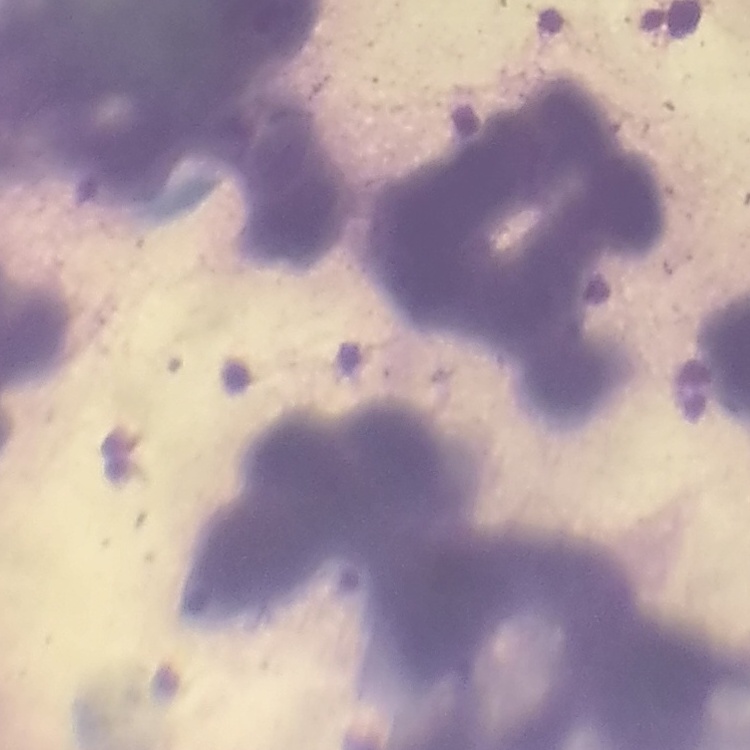
Summary:
  - Red blood cell morphology: rouleaux formation
  - Image type: square crop of a larger photomicrograph
  - Stain: Field's or Giemsa
  - Preparation: thin peripheral smear